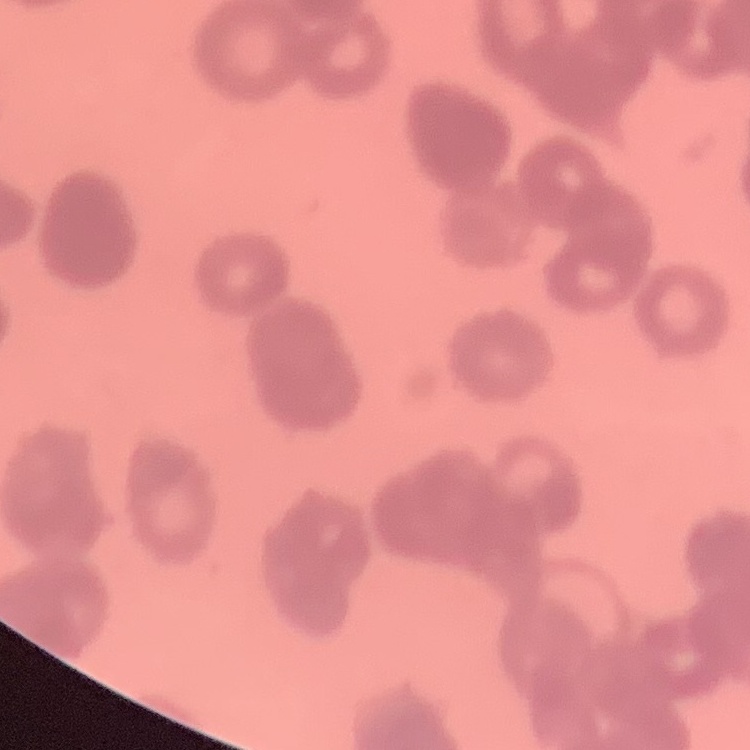 The red blood cells exhibit rouleaux formation. One tile cut from a larger photomicrograph. Thin peripheral smear. Stained with either Field's or Giemsa.